Assess this cell for malaria.
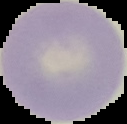

Uninfected.

Segmented cell region on a black background. From a thin blood smear. Image is 127×124 pixels.